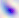
Summary:
  - Identification: Toxoplasma gondii
  - Modality: photomicrograph
  - Magnification: 400x